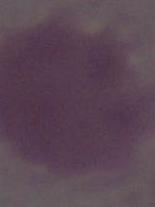
Summary:
  - Magnification: 1000x
  - Modality: photomicrograph
  - Identification: red blood cell